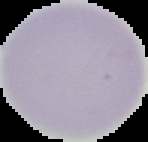
Summary:
  - Malaria status: uninfected
  - Image type: cell region segmented out of the field of view; surrounding area masked to black
  - Preparation: thin blood smear
  - Image size: 148×142 pixels